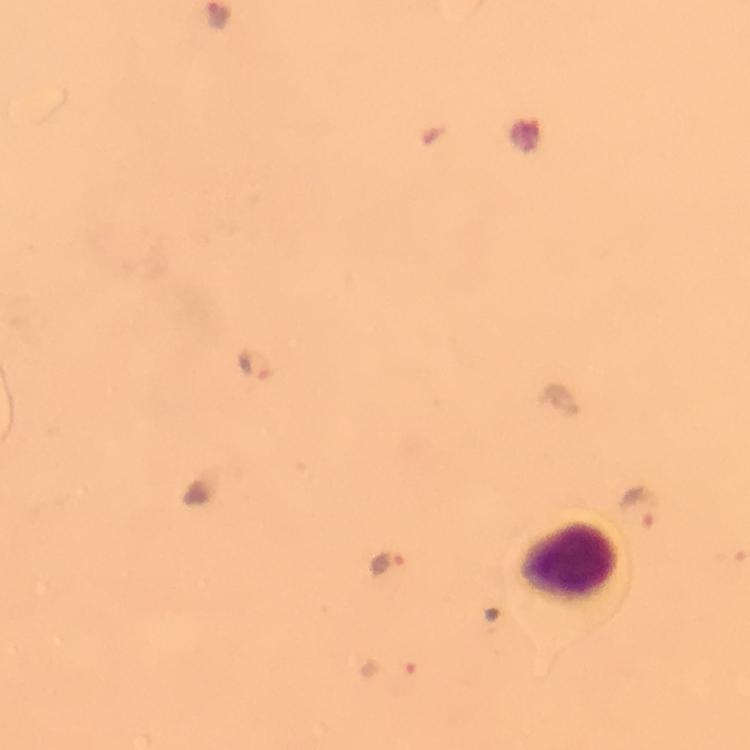 Approximate centers as (x, y) in pixels. Leukocyte locations: (578, 565). Plasmodium parasite locations: (256, 367), (640, 505), (388, 563), (387, 666). Smartphone photograph taken through a microscope. A crop from one field of view. Image is 750×750 pixels. Thick blood film. At 100x magnification. Giemsa stain. Immersion oil applied. From a diagnostic examination for malaria.